State the blood parasite species.
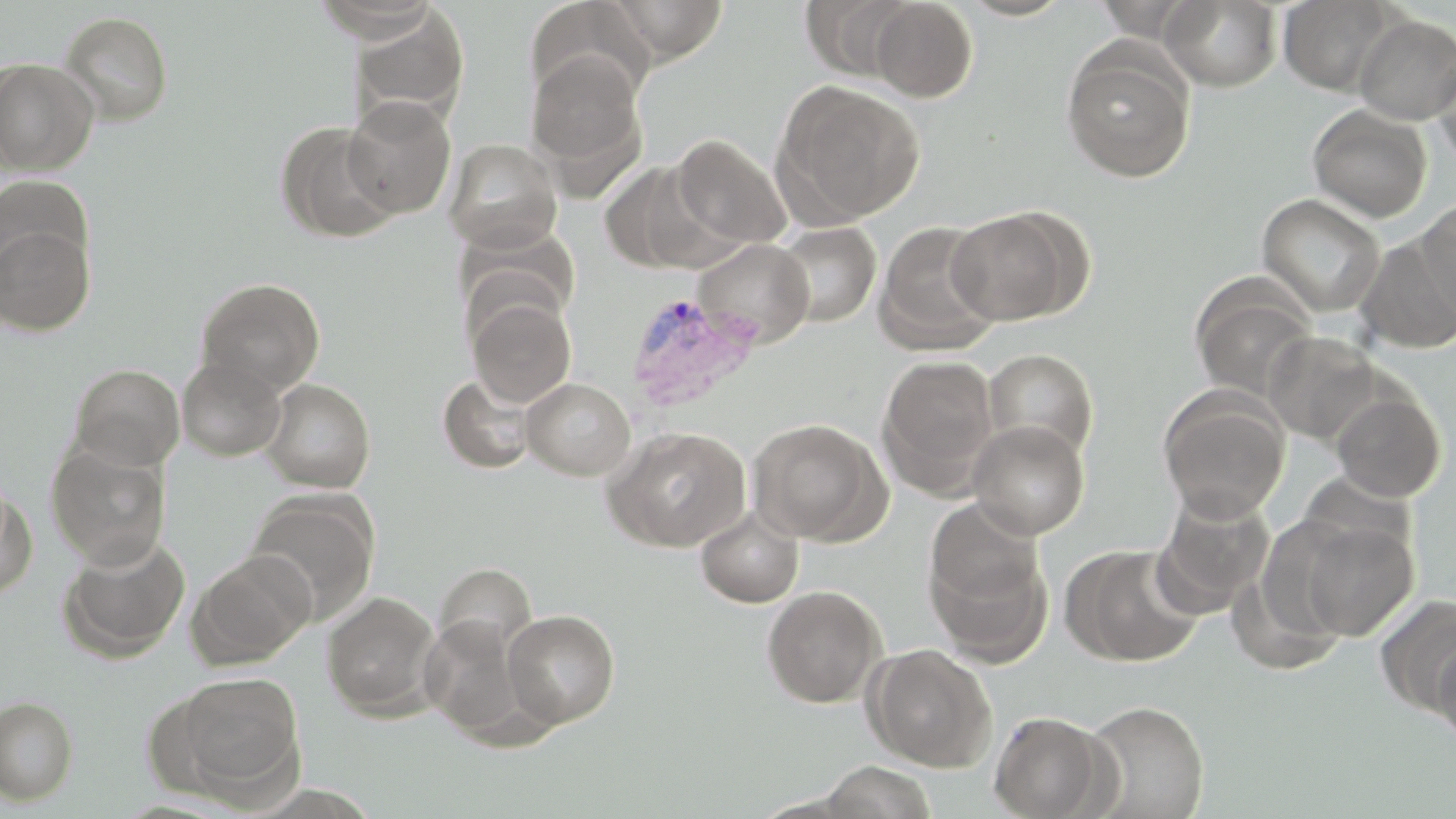

Plasmodium vivax.

Approximate bounding boxes as [x1, y1, x2, y2] in pixels. Plasmodium vivax-infected red blood cell locations: [625, 291, 764, 413]. Uninfected red blood cell locations: [313, 0, 441, 42], [603, 0, 730, 64], [801, 0, 916, 80], [869, 0, 978, 102], [955, 0, 1076, 21], [1161, 0, 1283, 91], [1278, 0, 1400, 95], [347, 6, 470, 125], [56, 10, 174, 125], [1353, 13, 1456, 124], [1060, 42, 1197, 183], [525, 49, 648, 184], [1431, 52, 1456, 171], [0, 58, 99, 176], [774, 80, 925, 225], [341, 97, 458, 219], [1307, 104, 1433, 223], [275, 121, 399, 244], [670, 134, 792, 251], [444, 138, 562, 253], [597, 159, 721, 273], [0, 175, 94, 284], [1257, 194, 1385, 317], [1415, 196, 1455, 327], [944, 208, 1084, 326], [875, 221, 1000, 352], [0, 222, 96, 335], [774, 222, 880, 327], [1353, 233, 1456, 355], [694, 238, 814, 348], [195, 277, 326, 394], [1189, 277, 1318, 401], [467, 295, 576, 407], [1263, 330, 1381, 443], [983, 348, 1098, 460], [876, 355, 999, 491], [177, 357, 287, 461], [69, 363, 185, 471], [437, 372, 537, 474], [522, 377, 635, 480], [261, 378, 375, 492], [1157, 388, 1289, 521], [1330, 390, 1447, 503], [748, 419, 886, 544], [968, 421, 1090, 539], [603, 426, 751, 552], [46, 443, 170, 568], [0, 481, 36, 602], [1152, 489, 1276, 612], [245, 491, 379, 624], [694, 506, 805, 608], [924, 508, 1052, 664], [1296, 518, 1418, 640], [57, 533, 191, 662], [1063, 544, 1206, 667], [188, 550, 316, 670], [434, 563, 536, 657], [761, 585, 886, 708], [321, 591, 443, 721], [1376, 593, 1456, 716], [502, 609, 620, 728], [420, 615, 536, 742], [1432, 636, 1456, 747], [863, 644, 997, 772], [162, 671, 306, 804], [0, 696, 78, 805], [1082, 700, 1210, 819], [988, 710, 1112, 818], [817, 761, 939, 818]. Image is 1456×819 pixels. 1000x magnification. Thin blood film. Light microscopy. May-Grünwald-Giemsa-stained preparation. One field of a larger specimen.